Assess this cell for malaria.
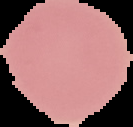

It is uninfected.

From a thin blood smear. Segmented cell region on a black background. Image is 133×127 pixels.